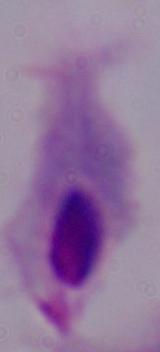

Photomicrograph. 1000x magnification. A trichomonad is shown.